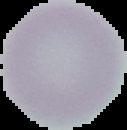

image_size: 127×130 pixels
preparation: thin blood smear
image_type: segmented cell region on a black background
malaria_status: uninfected